Comment on the morphology of the red blood cells.
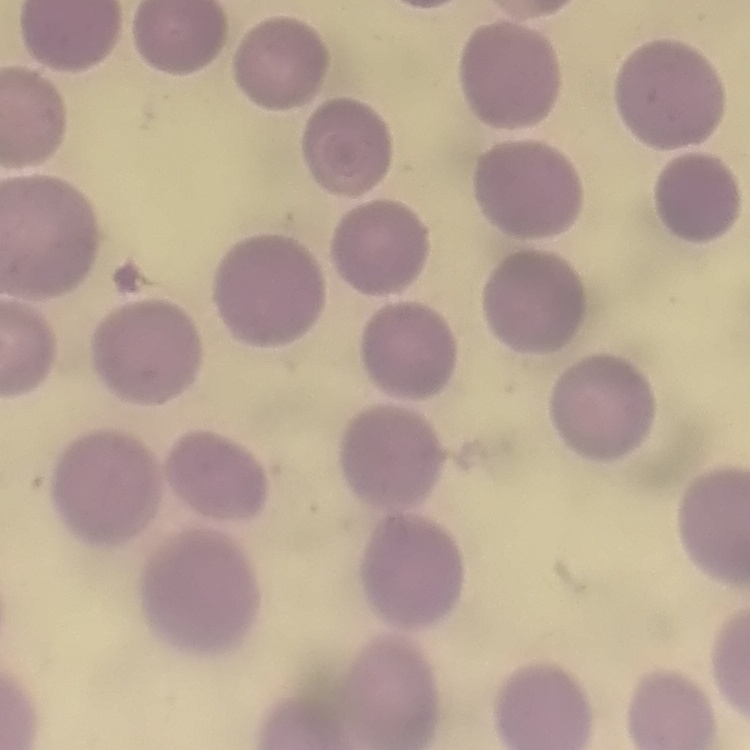

No rouleaux formation.

stain = Field's or Giemsa
preparation = thin peripheral smear
image type = square crop of a larger photomicrograph